State the preparation type.
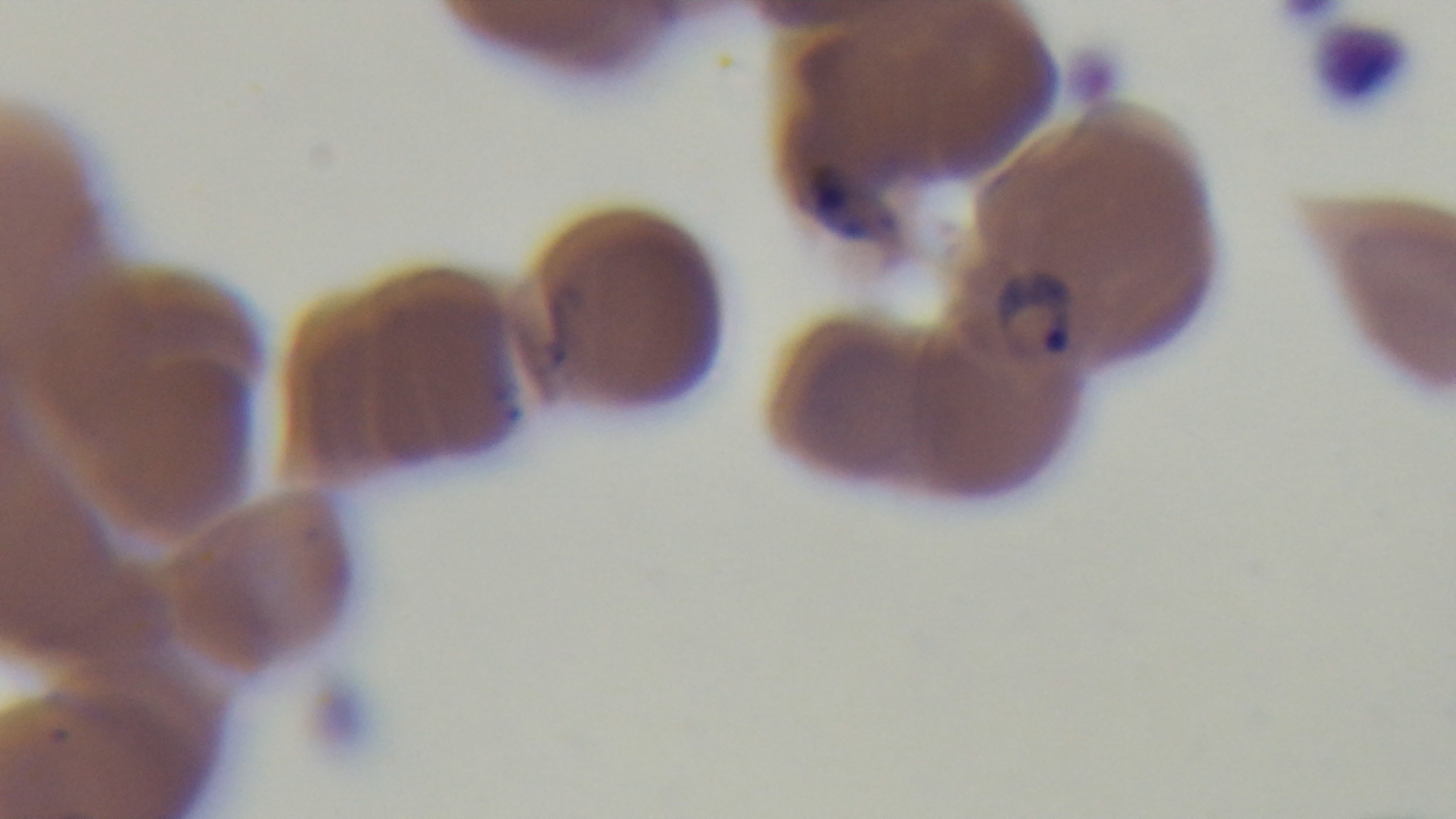

Thin.

Summary:
  - Malaria status: infected
  - Capture: mounted 4K digital camera
  - Modality: light microscopy
  - Stain: Giemsa
  - Objective: 100x oil immersion
  - Field of view: single